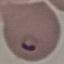

Summary:
  - Result: malaria parasites identified
  - Image type: automatically extracted cell patch, resized to 64 × 64 pixels
  - Capture: smartphone camera at the microscope eyepiece
  - Preparation: thin blood smear
  - Stain: Giemsa